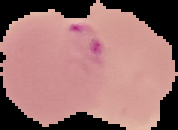 Image is 178×130 pixels. Segmented cell region on a black background. From a thin blood smear. Malaria status: parasitized.